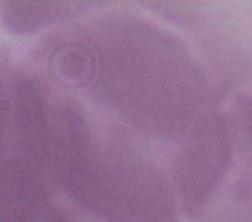

identification: red blood cell
magnification: 1000x
modality: photomicrograph